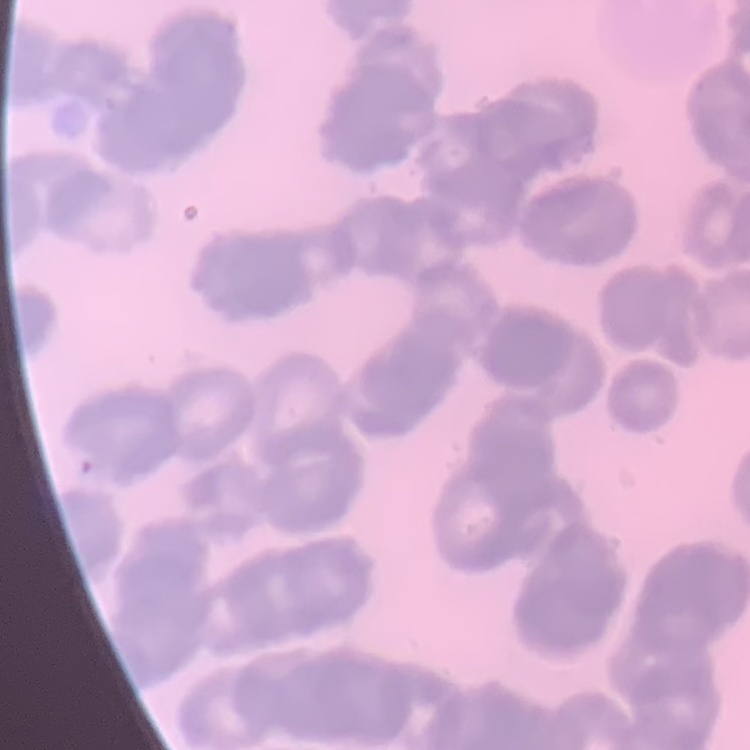

The erythrocytes show rouleaux formation. Thin blood smear. Stained with either Field's or Giemsa. One tile cut from a larger photomicrograph.